Assess the morphology of the red blood cells.
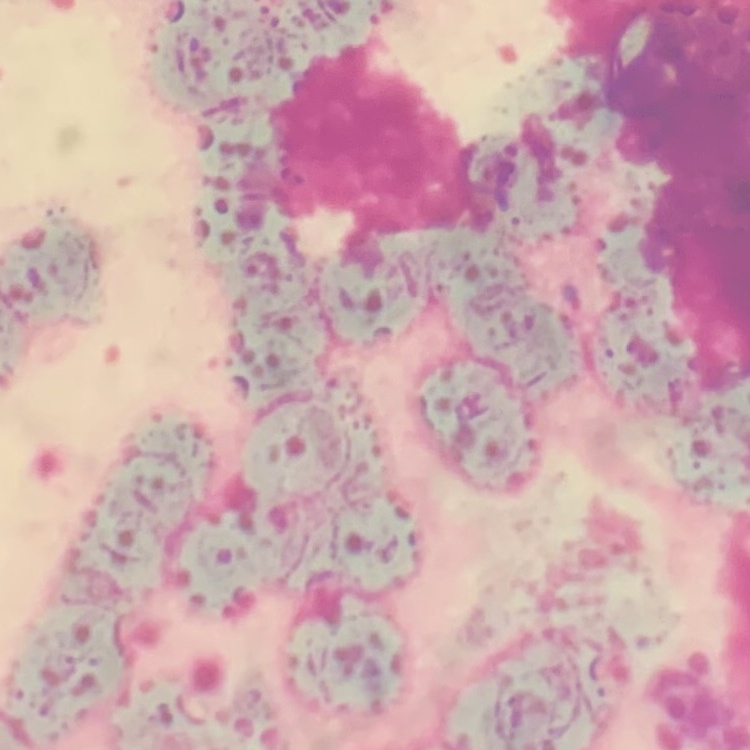

They show rouleaux formation.

Summary:
  - Stain: Field's or Giemsa
  - Image type: one tile cut from a larger photomicrograph
  - Preparation: thin blood film